Name the parasite shown.
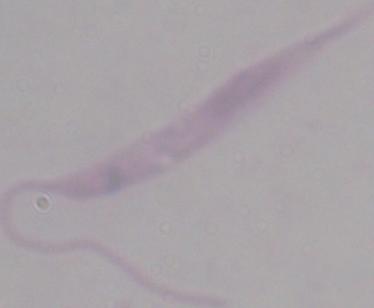

Leishmania.

modality: micrograph
magnification: 1000x